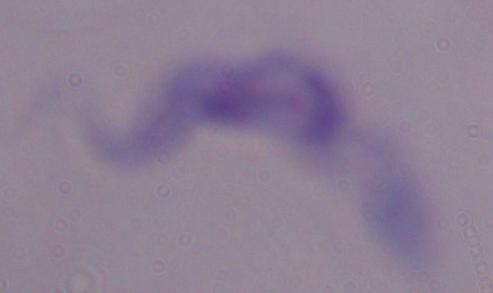 Photomicrograph. A trypanosome is shown. Captured at 1000x magnification.